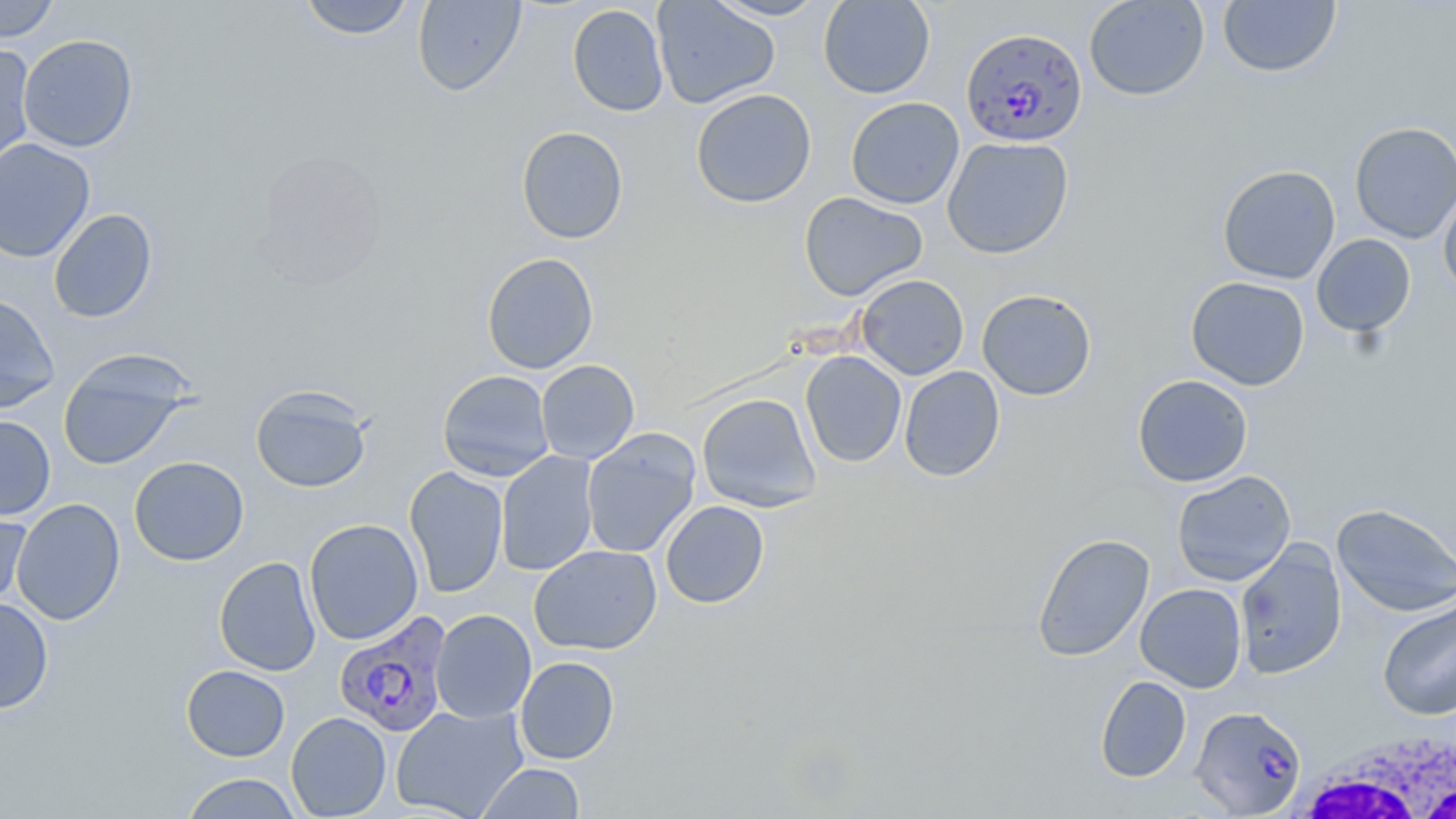

{
  "slide_level_diagnosis": "Plasmodium falciparum",
  "preparation": "thin blood film",
  "image_size": "1456×819 pixels",
  "plasmodium_falciparum_infected_red_blood_cell_locations": "approximate bounding boxes as (x1, y1, x2, y2) in pixels: (961, 27, 1088, 148), (334, 611, 453, 738), (1190, 705, 1307, 817)",
  "magnification": "1000x",
  "white_blood_cell_locations": "approximate bounding boxes as (x1, y1, x2, y2) in pixels: (1284, 733, 1456, 819)",
  "modality": "optical microscopy",
  "stain": "May-Grünwald-Giemsa",
  "uninfected_red_blood_cell_locations": "approximate bounding boxes as (x1, y1, x2, y2) in pixels: (0, 0, 59, 44), (297, 0, 416, 40), (412, 0, 526, 97), (651, 0, 780, 109), (708, 0, 829, 21), (818, 0, 935, 99), (1083, 0, 1210, 101), (1217, 1, 1341, 78), (567, 4, 669, 116), (18, 34, 138, 152), (0, 42, 37, 174), (690, 88, 817, 208), (846, 97, 964, 209), (1350, 121, 1456, 244), (516, 126, 629, 243), (942, 136, 1074, 259), (0, 138, 96, 263), (252, 150, 390, 288), (1217, 164, 1341, 285), (1439, 186, 1456, 298), (798, 192, 929, 301), (48, 208, 158, 323), (1311, 234, 1416, 337), (482, 252, 599, 374), (856, 274, 969, 380), (1185, 276, 1310, 391), (977, 289, 1097, 401), (0, 293, 60, 414), (57, 350, 194, 470), (800, 350, 907, 468), (535, 360, 640, 464), (899, 366, 1004, 482), (437, 369, 555, 481), (1132, 374, 1253, 487), (250, 384, 372, 493), (696, 392, 822, 513), (0, 415, 56, 519), (581, 428, 701, 559), (496, 451, 599, 576), (129, 456, 249, 566), (404, 466, 509, 598), (1171, 470, 1296, 587), (11, 498, 126, 626), (1, 500, 33, 610), (660, 501, 770, 608), (1331, 503, 1456, 617), (303, 518, 423, 645), (1031, 533, 1155, 661), (1233, 540, 1348, 680), (529, 544, 662, 655), (214, 556, 321, 677), (1135, 583, 1247, 692), (0, 597, 54, 714), (1377, 600, 1456, 720), (430, 609, 536, 723), (515, 656, 620, 764), (181, 664, 290, 761), (1094, 675, 1191, 782), (391, 704, 528, 818), (286, 712, 391, 818), (478, 762, 586, 818), (180, 772, 302, 818)",
  "field_of_view": "one of a larger specimen"
}